Identify the parasite.
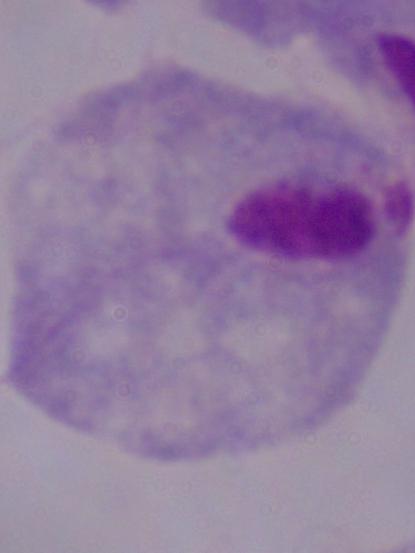
A trichomonad.

Summary:
  - Modality: micrograph
  - Magnification: 1000x